Identify the preparation type.
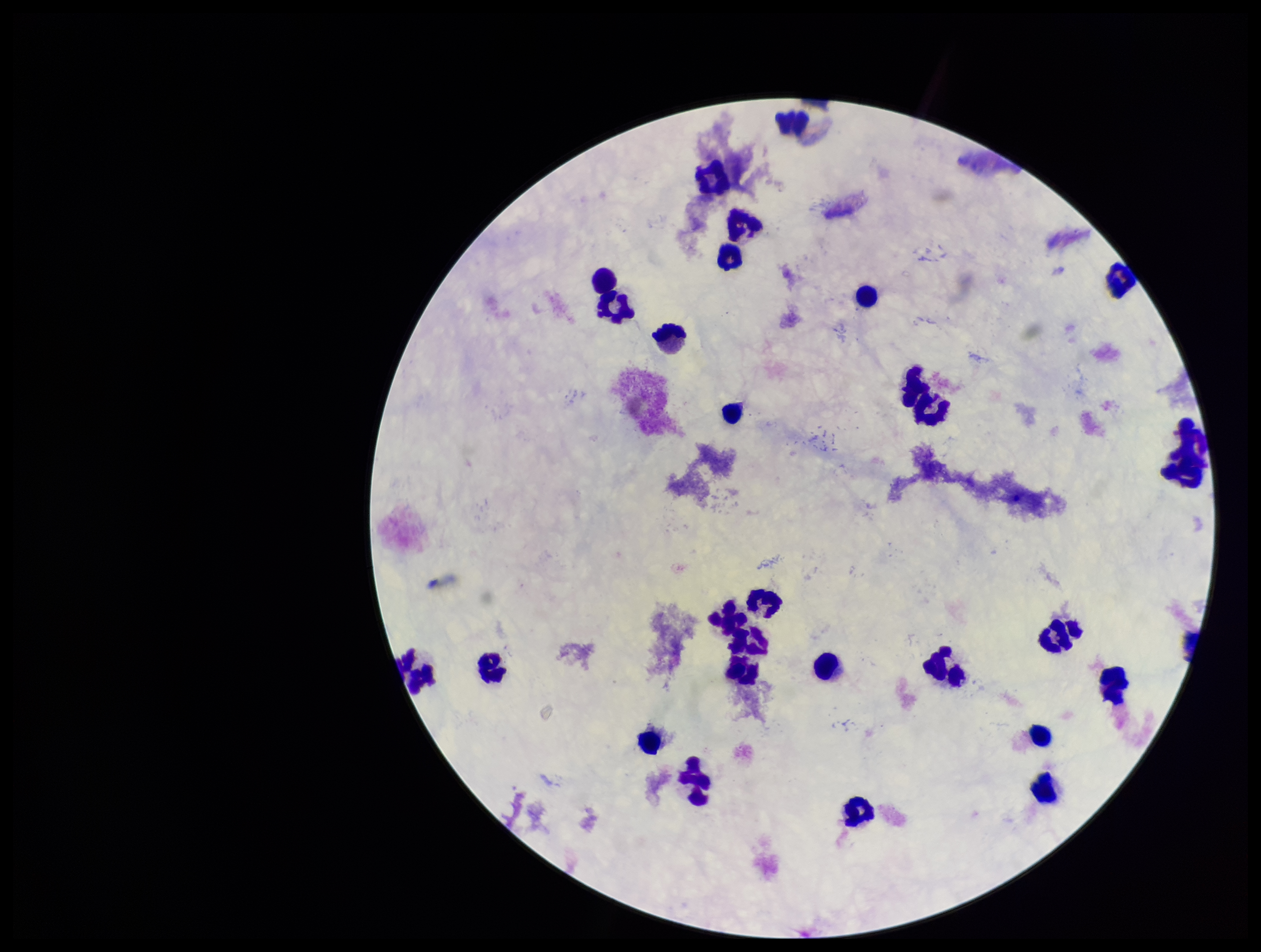
Thick.

Leukocyte count: 28. Plasmodium parasites: none seen. Patient malaria status: negative. Stained with Giemsa. Smartphone photograph taken through the eyepiece of a microscope. One field from this slide. Parasite count: 0. Image is 1261×952 pixels.